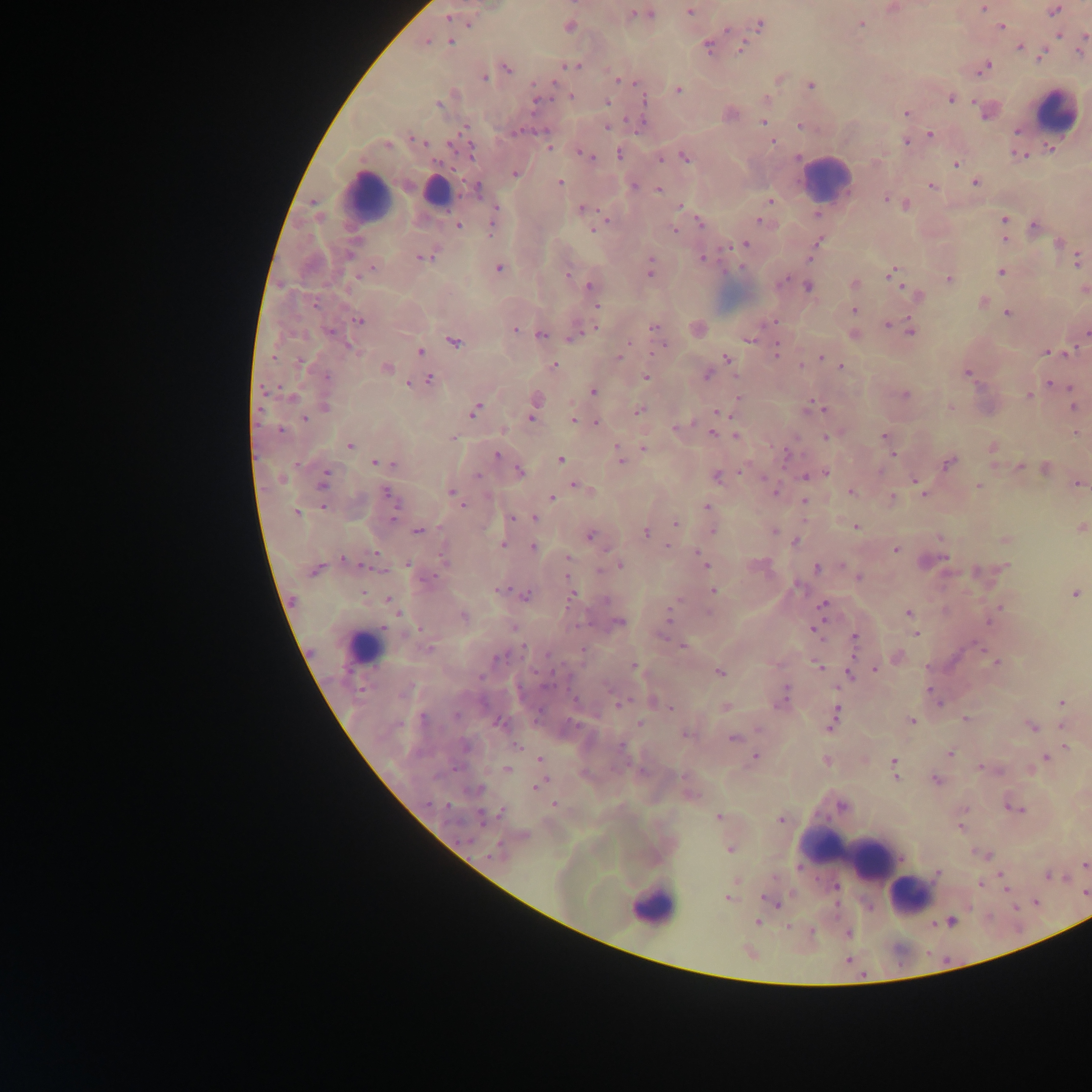

Approximate centers as [x, y] in pixels.
Summary:
  - Leukocyte locations: [1057, 111], [825, 177], [435, 192], [366, 195], [363, 648], [850, 850], [909, 895], [652, 907]
  - Malaria parasite locations: [983, 8], [1054, 11], [690, 12], [639, 14], [646, 14], [448, 18], [861, 24], [760, 25], [569, 27], [1001, 27], [727, 29], [1058, 34], [1084, 41], [427, 42], [451, 42], [708, 46], [742, 48], [1019, 48], [1082, 48], [1041, 56], [572, 66], [985, 66], [507, 68], [484, 79], [620, 80], [810, 86], [679, 90], [571, 96], [950, 98], [643, 100], [536, 101], [607, 102], [438, 104], [986, 112], [906, 113], [730, 114], [763, 121], [799, 125], [607, 127], [518, 131], [1017, 131], [931, 135], [416, 140], [772, 142], [906, 142], [388, 145], [548, 147], [467, 148], [620, 154], [587, 156], [1019, 156], [685, 157], [798, 158], [661, 159], [956, 164], [516, 173], [559, 183], [975, 183], [634, 186], [931, 186], [477, 189], [658, 189], [887, 199], [770, 200], [896, 202], [906, 205], [680, 206], [582, 209], [818, 215], [1004, 219], [761, 220], [492, 222], [701, 224], [457, 226], [600, 226], [1035, 226], [594, 229], [675, 230], [1004, 239], [817, 243], [1059, 243], [745, 244], [348, 254], [424, 257], [702, 259], [1077, 260], [650, 267], [372, 268], [499, 268], [1001, 272], [567, 273], [893, 273], [948, 279], [783, 281], [854, 284], [590, 286], [809, 287], [916, 294], [983, 302], [315, 304], [597, 306], [854, 310], [1008, 313], [359, 321], [889, 325], [654, 327], [515, 330], [330, 332], [911, 332], [1085, 333], [541, 335], [854, 335], [572, 337], [750, 339], [454, 342], [349, 346], [662, 346], [626, 347], [777, 350], [420, 351], [1068, 351], [1048, 352], [620, 355], [823, 357], [727, 359], [300, 362], [553, 366], [841, 367], [386, 369], [967, 374], [707, 375], [327, 377], [645, 377], [429, 379], [1050, 383], [409, 384], [593, 391], [905, 395], [1028, 396], [292, 397], [536, 402], [1074, 406], [325, 407], [816, 407], [951, 408], [639, 410], [474, 411], [717, 411], [532, 417], [304, 419], [573, 419], [596, 423], [677, 428], [280, 430], [502, 430], [713, 433], [884, 435], [736, 436], [453, 437], [826, 437], [349, 445], [644, 448], [993, 448], [787, 455], [497, 456], [620, 457], [560, 460], [376, 463], [386, 464], [395, 464], [948, 464], [1019, 466], [1045, 469], [520, 471], [824, 473], [477, 476], [716, 476], [807, 477], [282, 479], [323, 481], [917, 481], [575, 484], [1078, 484], [978, 485], [773, 490], [850, 491], [922, 491], [452, 492], [388, 494], [552, 498], [892, 498], [804, 500], [706, 507], [324, 508], [296, 512], [512, 518], [535, 518], [392, 519], [675, 524], [856, 526], [1082, 527], [713, 530], [418, 532], [774, 532], [646, 533], [591, 536], [1005, 540], [796, 541], [503, 545], [533, 547], [895, 550], [375, 554], [443, 557], [568, 558], [945, 559], [345, 560], [702, 561], [408, 564], [619, 565], [1006, 567], [817, 568], [315, 570], [859, 577], [797, 586], [500, 590], [713, 591], [1074, 594], [526, 595], [572, 596], [389, 600], [605, 600], [822, 607], [998, 608], [708, 612], [909, 613], [464, 616], [669, 618], [990, 620], [619, 622], [514, 628], [815, 629], [914, 633], [663, 634], [854, 637], [684, 646], [429, 649], [897, 656], [500, 658], [997, 663], [818, 666], [634, 667], [876, 669], [720, 672], [850, 675], [784, 696], [934, 696], [938, 701], [781, 702], [621, 703], [1062, 703], [670, 708], [456, 716], [423, 719], [965, 719], [832, 720], [912, 721], [499, 724], [640, 724], [1032, 726], [687, 736], [733, 738], [517, 745], [622, 746], [1066, 746], [950, 753], [755, 758], [1045, 758], [539, 759], [826, 761], [894, 764], [982, 767], [508, 769], [936, 780], [540, 785], [554, 805], [842, 806], [1016, 809], [502, 812], [484, 816], [718, 817], [781, 820], [961, 827], [729, 850], [494, 853], [983, 854], [1085, 865], [937, 873], [1048, 876], [736, 881], [980, 884], [1085, 894], [729, 899], [770, 901], [951, 921], [758, 922], [848, 934]
  - Image size: 1092×1092 pixels
  - Field of view: single
  - Country: Ghana
  - Capture: mobile-phone photograph through a microscope
  - Preparation: thick blood film